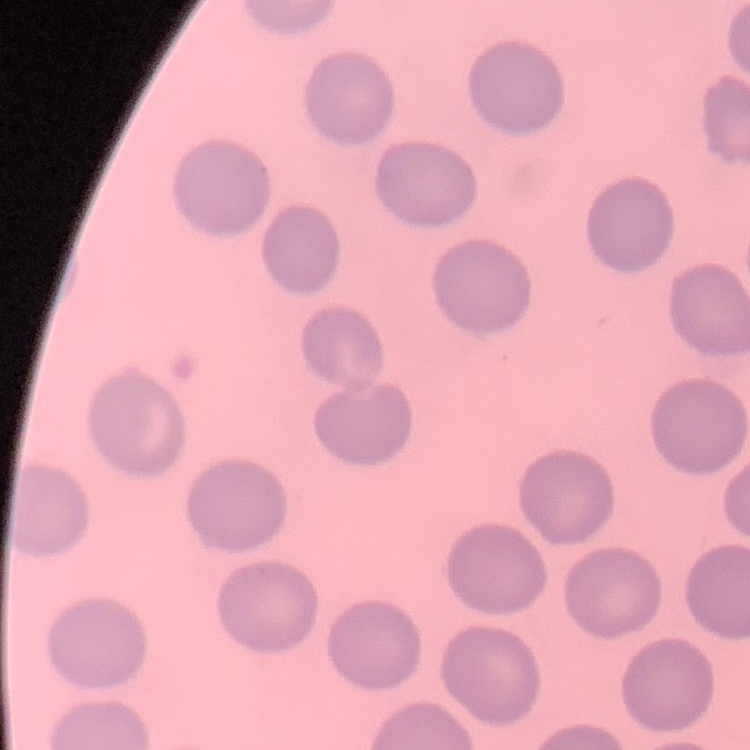

The red blood cells show no rouleaux formation. Thin blood smear. Square crop of a larger photomicrograph. Stained with either Field's or Giemsa.